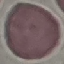 Malaria status: uninfected. Acquired by smartphone through the microscope eyepiece. Thin smear of blood. Cell patch, automatically extracted from a larger field of view and resized to 64 × 64 pixels. Giemsa stain.